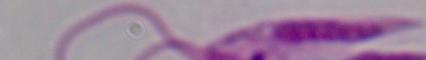

modality: photomicrograph
identification: Leishmania
magnification: 1000x